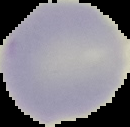

Cell region segmented out of the field of view; the surrounding area is masked to black. Image is 130×127 pixels. Malaria status: uninfected. From a thin blood film.